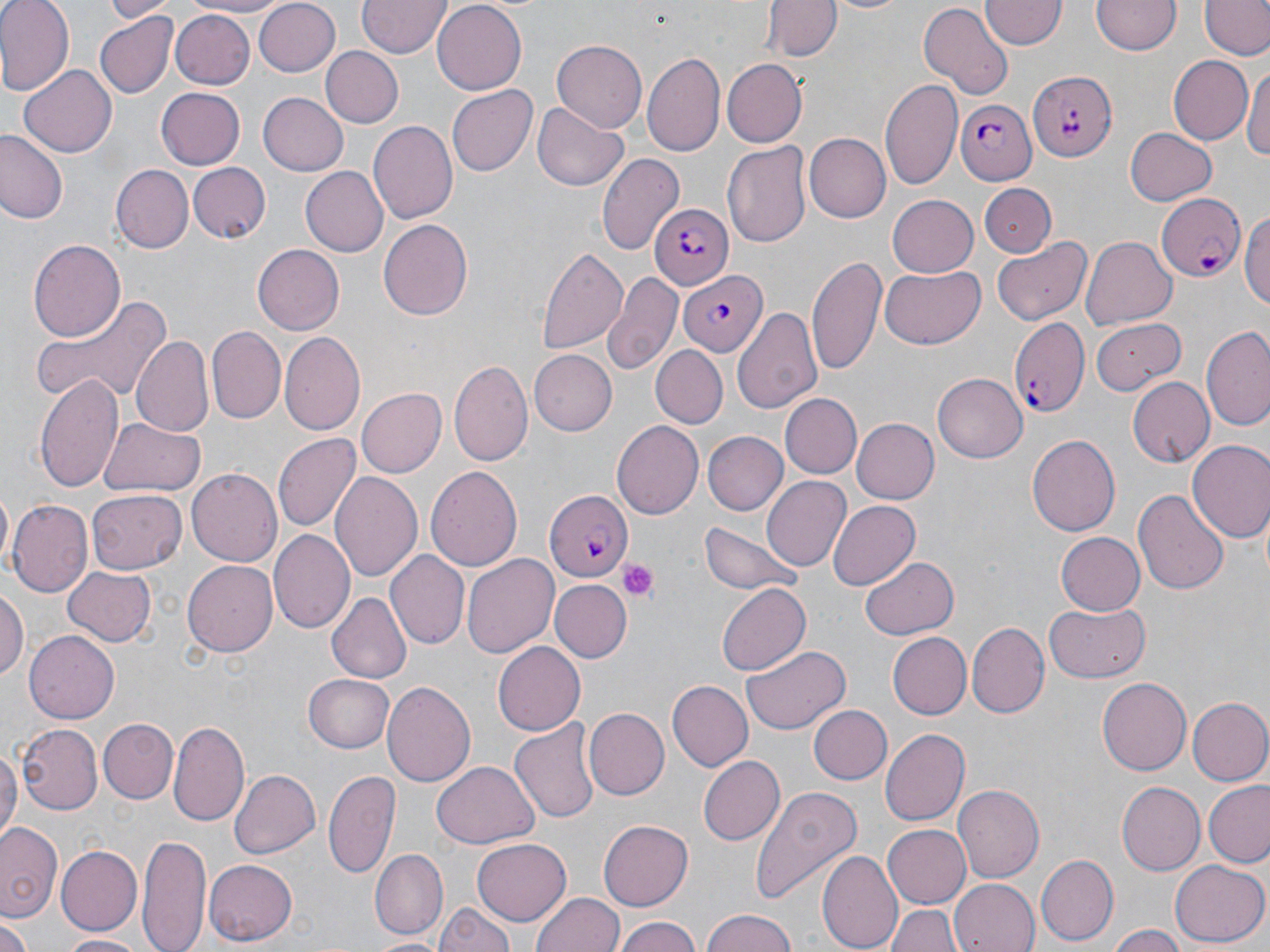 Approximate bounding boxes as (x1, y1, x2, y2) in pixels. Platelet locations: (619, 559, 661, 603). Plasmodium falciparum-infected red blood cell locations: (1026, 70, 1117, 160), (953, 100, 1036, 184), (1157, 192, 1247, 282), (647, 203, 734, 291), (678, 270, 766, 356), (1011, 317, 1090, 419), (544, 490, 634, 579). Uninfected red blood cell locations: (0, 0, 72, 96), (103, 0, 174, 21), (183, 0, 288, 18), (253, 0, 341, 78), (432, 0, 527, 91), (765, 0, 840, 61), (823, 0, 914, 15), (1091, 0, 1183, 56), (356, 1, 450, 59), (916, 1, 1012, 97), (981, 1, 1065, 51), (1202, 1, 1268, 60), (169, 10, 256, 88), (94, 12, 178, 100), (550, 40, 648, 132), (318, 45, 402, 129), (645, 51, 724, 159), (1168, 55, 1254, 145), (724, 60, 807, 147), (1243, 60, 1270, 165), (19, 64, 117, 156), (879, 77, 963, 189), (155, 87, 246, 170), (448, 87, 537, 177), (257, 91, 348, 176), (533, 101, 630, 192), (370, 119, 458, 225), (1123, 127, 1217, 204), (0, 132, 68, 226), (804, 133, 891, 224), (723, 141, 812, 246), (595, 153, 683, 254), (186, 163, 270, 242), (110, 164, 192, 252), (300, 166, 387, 257), (980, 183, 1058, 256), (885, 196, 977, 278), (1242, 206, 1270, 315), (376, 219, 471, 320), (1081, 236, 1178, 329), (992, 237, 1091, 323), (27, 239, 126, 341), (535, 245, 628, 357), (253, 246, 343, 335), (807, 253, 887, 375), (880, 266, 987, 349), (605, 275, 683, 374), (31, 295, 170, 408), (734, 306, 823, 416), (1089, 317, 1186, 395), (1200, 327, 1270, 430), (207, 328, 286, 427), (280, 332, 365, 433), (133, 335, 215, 438), (651, 346, 728, 428), (529, 350, 616, 435), (450, 361, 532, 467), (35, 374, 123, 491), (933, 374, 1027, 463), (1128, 376, 1212, 466), (357, 388, 447, 477), (780, 393, 861, 477), (99, 417, 202, 497), (851, 418, 938, 504), (612, 421, 704, 521), (702, 432, 787, 516), (272, 434, 358, 531), (1026, 434, 1120, 539), (1190, 440, 1270, 543), (424, 466, 524, 573), (186, 469, 281, 566), (329, 470, 421, 581), (760, 477, 849, 570), (87, 488, 185, 573), (1133, 488, 1230, 593), (9, 501, 92, 596), (829, 501, 918, 589), (698, 522, 805, 597), (268, 529, 354, 635), (1057, 532, 1145, 615), (385, 552, 469, 649), (462, 553, 559, 655), (861, 555, 960, 641), (183, 561, 278, 655), (63, 567, 156, 647), (552, 581, 630, 663), (714, 583, 810, 677), (0, 588, 26, 684), (328, 592, 411, 684), (1045, 602, 1148, 682), (967, 621, 1049, 718), (24, 632, 118, 724), (885, 632, 971, 719), (493, 641, 589, 735), (742, 646, 851, 736), (303, 674, 394, 753), (1096, 676, 1191, 775), (666, 681, 751, 771), (383, 682, 475, 787), (1186, 697, 1270, 787), (808, 703, 891, 783), (583, 708, 669, 801), (96, 718, 177, 803), (169, 719, 249, 825), (512, 719, 601, 825), (18, 723, 100, 814), (881, 729, 970, 825), (0, 746, 20, 844), (697, 755, 784, 846), (429, 762, 537, 849), (230, 768, 321, 860), (324, 768, 400, 879), (1205, 782, 1270, 868), (954, 783, 1045, 882), (1118, 783, 1204, 875), (749, 787, 859, 906), (599, 819, 693, 908), (1, 823, 63, 921), (882, 824, 971, 909), (138, 836, 209, 952), (472, 838, 570, 924), (56, 844, 142, 935), (372, 848, 447, 939), (820, 849, 901, 952), (1035, 855, 1118, 944), (201, 859, 297, 945), (1168, 859, 1268, 948), (948, 879, 1038, 952), (533, 893, 624, 952), (436, 899, 515, 952), (886, 904, 961, 952), (701, 912, 802, 952), (613, 916, 706, 952), (1, 921, 31, 952), (1107, 926, 1188, 952), (59, 932, 152, 949), (365, 935, 450, 951). Slide-level diagnosis: Plasmodium falciparum. Captured at 1000x magnification. May-Grünwald-Giemsa stain. Light microscopy. Image is 1270×952 pixels. Single field of view. Thin blood smear.